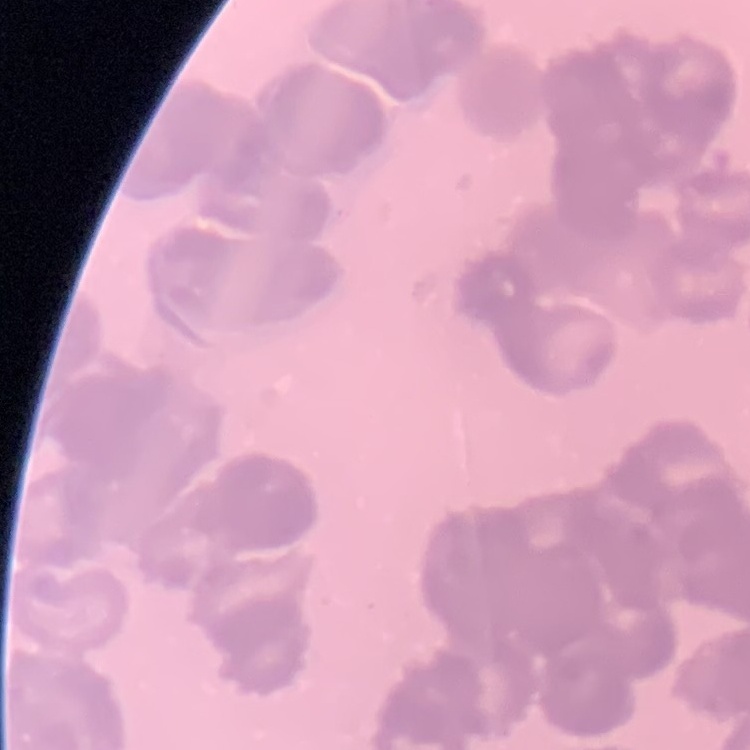

The red blood cells show rouleaux formation. Square crop of a larger photomicrograph. Field's or Giemsa stain. Thin peripheral smear.